Identify the parasite.
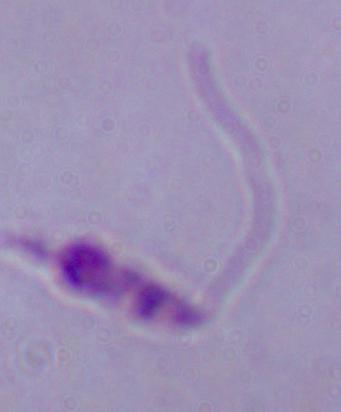

This is Leishmania.

Micrograph. Captured at 1000x magnification.